Assess the morphology of the erythrocytes.
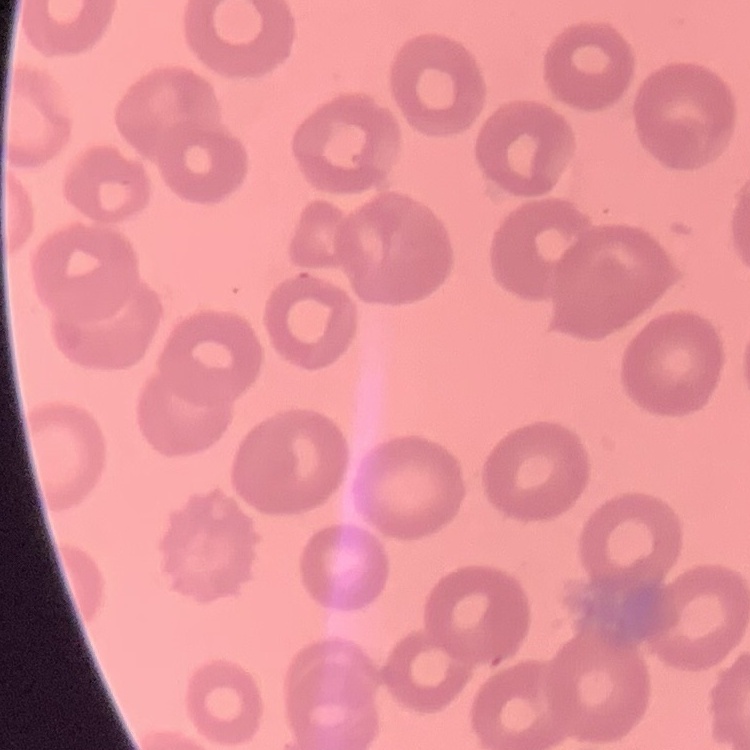
No rouleaux formation.

Summary:
  - Stain: Field's or Giemsa
  - Image type: square crop of a larger photomicrograph
  - Preparation: thin blood film